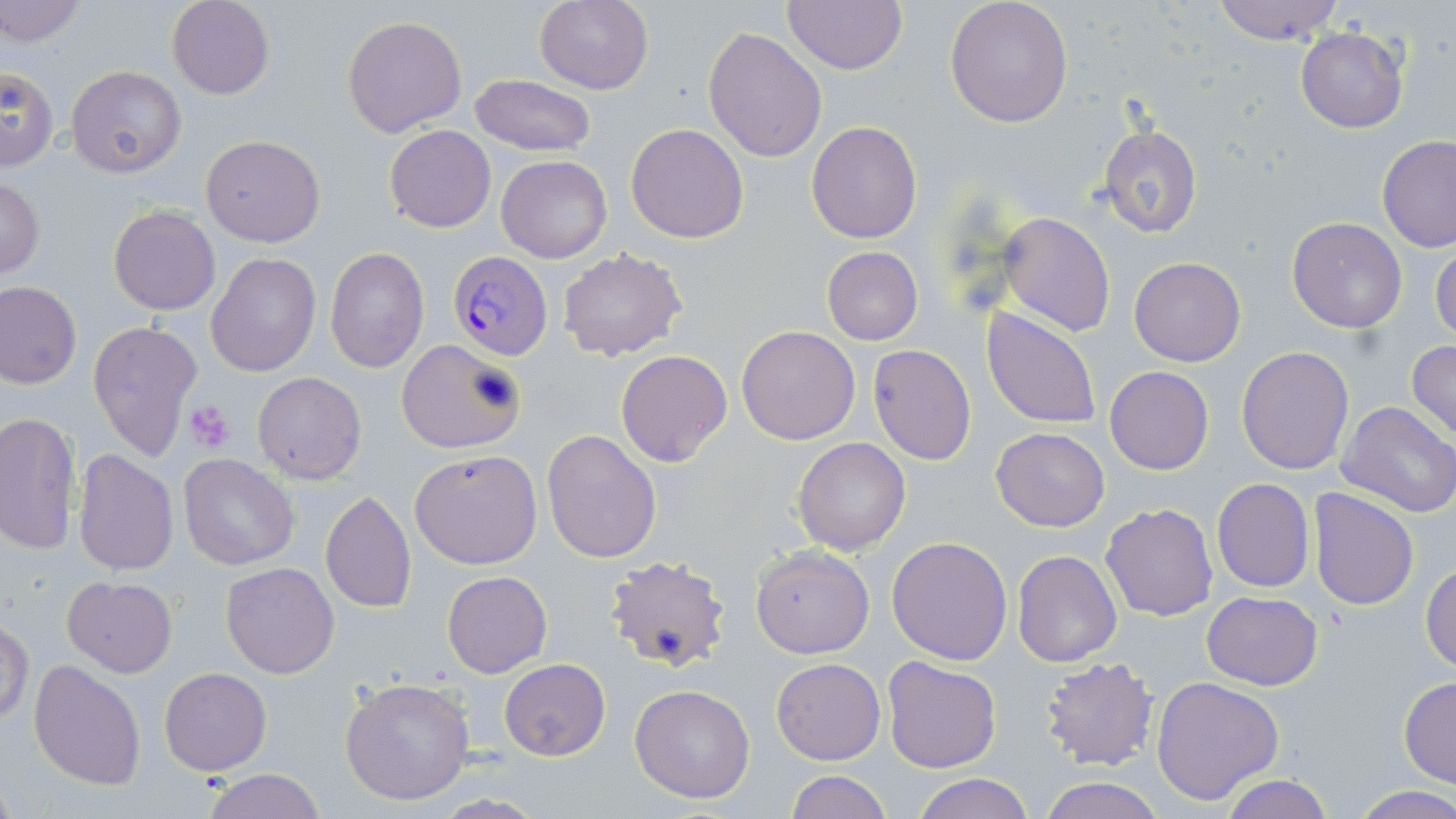 Approximate bounding boxes as [x1, y1, x2, y2] in pixels. Platelet locations: [463, 359, 524, 421], [185, 401, 236, 452]. Uninfected red blood cell locations: [0, 0, 87, 50], [167, 0, 273, 99], [533, 0, 654, 95], [783, 0, 908, 75], [944, 0, 1074, 127], [1209, 0, 1346, 44], [342, 14, 467, 138], [702, 25, 828, 162], [1295, 28, 1408, 133], [0, 65, 58, 171], [66, 65, 187, 178], [469, 74, 594, 156], [806, 120, 922, 244], [625, 123, 749, 244], [1097, 123, 1204, 240], [385, 126, 495, 232], [201, 135, 326, 247], [1377, 135, 1456, 253], [495, 155, 612, 263], [0, 177, 47, 281], [108, 206, 220, 315], [998, 210, 1115, 336], [1286, 217, 1407, 333], [1431, 240, 1456, 345], [821, 246, 924, 346], [326, 247, 429, 373], [557, 248, 687, 362], [205, 253, 320, 375], [1129, 257, 1245, 367], [0, 280, 82, 389], [981, 306, 1103, 430], [88, 318, 204, 462], [735, 326, 860, 445], [395, 339, 527, 454], [1407, 339, 1456, 445], [868, 345, 976, 465], [1237, 346, 1354, 474], [615, 350, 732, 466], [1104, 366, 1215, 476], [252, 371, 367, 484], [1335, 401, 1456, 520], [0, 412, 80, 555], [990, 427, 1110, 530], [542, 428, 664, 563], [792, 437, 910, 556], [409, 448, 543, 570], [72, 449, 179, 576], [179, 454, 300, 571], [1211, 478, 1314, 593], [1307, 487, 1419, 610], [321, 490, 417, 613], [1101, 502, 1218, 620], [886, 535, 1014, 664], [750, 545, 874, 659], [1013, 549, 1122, 666], [605, 554, 733, 674], [1420, 560, 1456, 672], [220, 562, 339, 678], [442, 571, 552, 678], [62, 576, 178, 677], [1201, 591, 1323, 690], [1, 619, 34, 726], [1037, 654, 1157, 772], [881, 656, 1001, 773], [771, 657, 886, 766], [499, 658, 611, 760], [29, 661, 145, 791], [159, 667, 272, 774], [1151, 675, 1284, 805], [1398, 676, 1456, 789], [340, 678, 476, 807], [629, 683, 757, 803], [201, 769, 327, 819], [786, 771, 891, 819], [912, 774, 1033, 819], [1220, 775, 1336, 819], [1039, 777, 1164, 819], [1348, 784, 1456, 818], [427, 794, 550, 817]. Plasmodium falciparum-infected red blood cell locations: [448, 252, 553, 359]. Slide-level diagnosis: Plasmodium falciparum. Optical microscopy. Thin blood film. 1000x magnification. Image is 1456×819 pixels. Single field of view. May-Grünwald-Giemsa-stained preparation.